Identify the parasite.
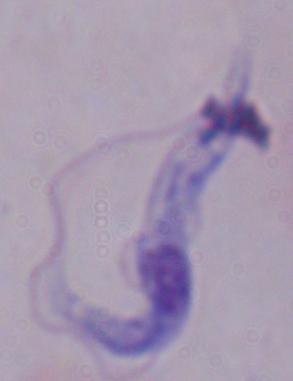
A trypanosome.

{
  "modality": "photomicrograph",
  "magnification": "1000x"
}